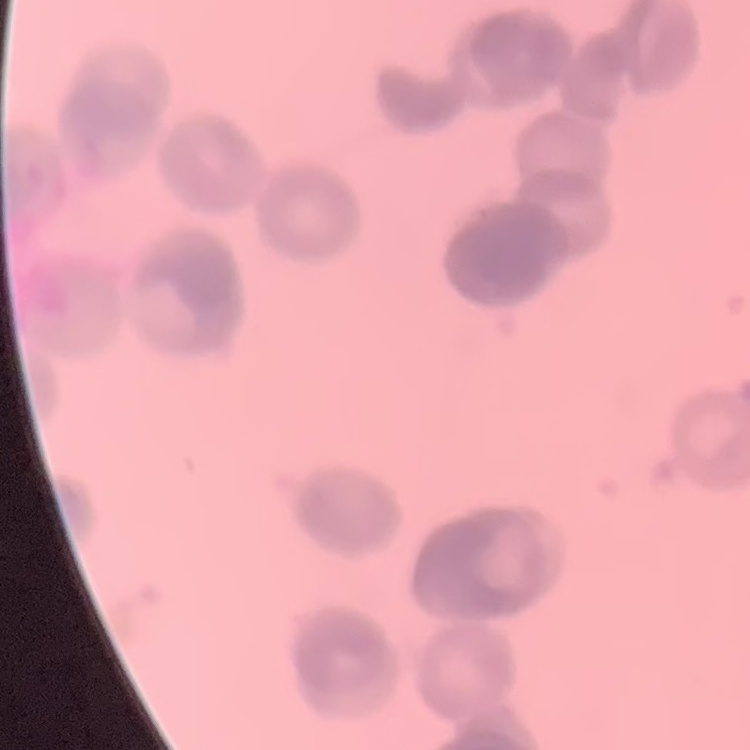
erythrocyte morphology = rouleaux formation
preparation = thin blood smear
image type = one tile cut from a larger photomicrograph
stain = Field's or Giemsa